Identify the parasite.
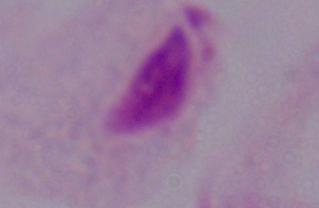
A trichomonad.

Photomicrograph. Captured at 1000x magnification.